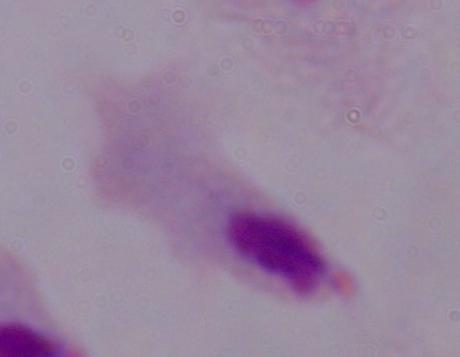
Summary:
  - Magnification: 1000x
  - Modality: photomicrograph
  - Identification: trichomonad